Classify this cell by malaria status.
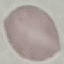
It is uninfected.

Photographed with a smartphone camera at the microscope eyepiece. Thin smear of blood. Giemsa-stained preparation. Automatically extracted cell patch, resized to 64 × 64 pixels.